Locate every Trypanosoma brucei.
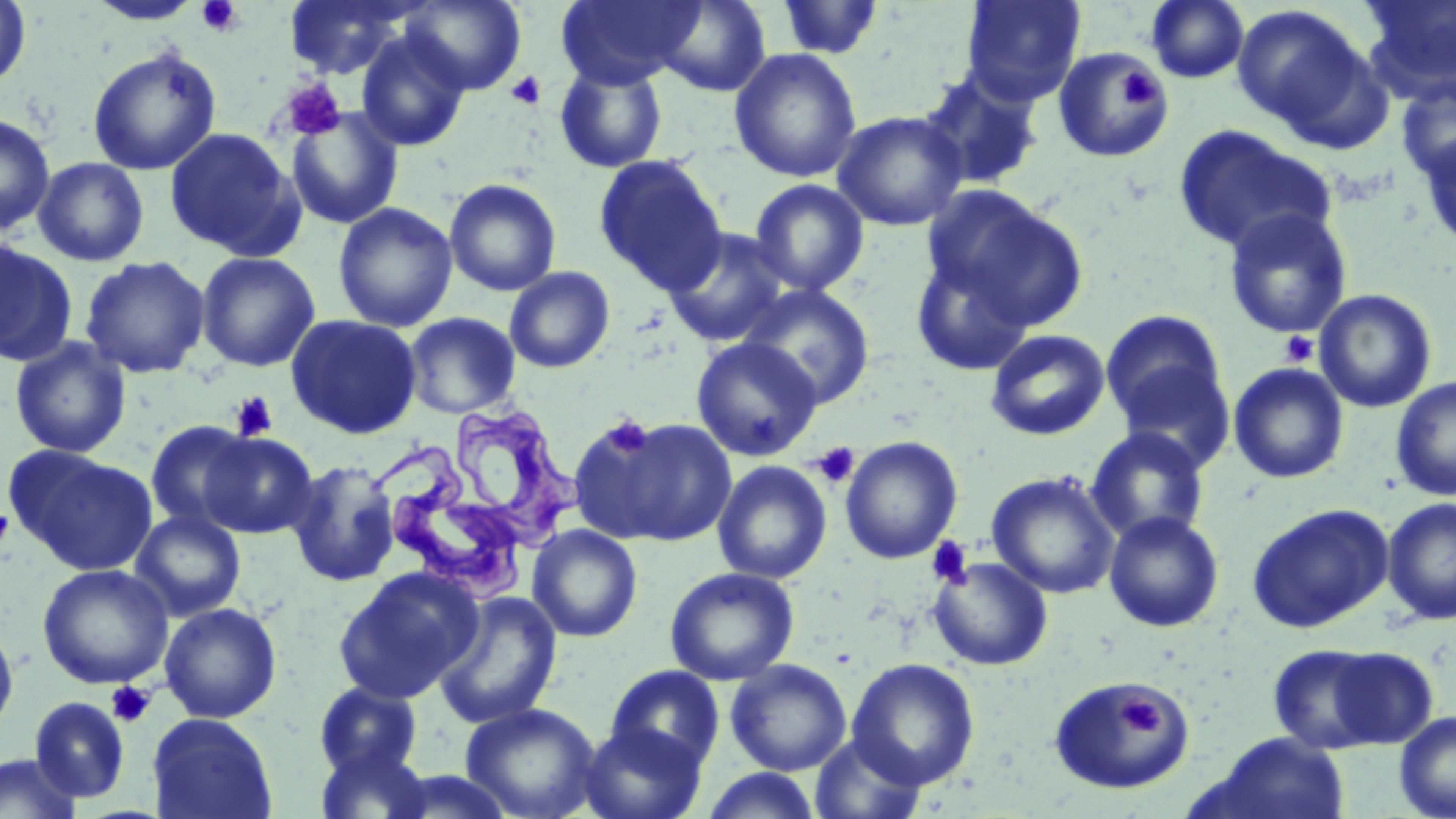
Approximate bounding boxes as (x1,y1)-(x2,y2) corner pairs in pixels.
Trypanosoma brucei: (440,410)-(585,556), (375,445)-(529,608).

slide-level diagnosis = Trypanosoma brucei
preparation = thin blood film
magnification = 1000x
platelet locations = approximate bounding boxes as (x1,y1)-(x2,y2) corner pairs in pixels: (196,0)-(243,37), (1116,67)-(1166,109), (505,70)-(547,110), (280,78)-(346,141), (1279,331)-(1319,367), (230,392)-(278,442), (601,416)-(653,459), (812,442)-(860,488), (0,506)-(15,551), (926,537)-(973,589), (107,682)-(155,728), (1120,696)-(1161,736)
modality = light microscopy
stain = May-Grünwald-Giemsa
field of view = one of a larger specimen
uninfected red blood cell locations = approximate bounding boxes as (x1,y1)-(x2,y2) corner pairs in pixels: (0,0)-(32,91), (86,0)-(205,25), (283,0)-(418,80), (400,0)-(527,95), (557,0)-(701,88), (653,0)-(771,97), (776,0)-(885,60), (960,0)-(1086,105), (1146,0)-(1249,84), (1359,0)-(1456,101), (1232,5)-(1377,140), (356,30)-(470,151), (87,46)-(221,176), (1052,47)-(1174,163), (729,48)-(862,183), (554,61)-(668,173), (916,69)-(1046,191), (1395,73)-(1456,186), (285,107)-(404,229), (832,110)-(968,232), (0,113)-(55,235), (1172,125)-(1334,256), (163,127)-(303,260), (1416,128)-(1456,254), (593,154)-(728,295), (33,157)-(150,267), (443,178)-(562,296), (750,179)-(869,297), (923,185)-(1088,331), (333,202)-(458,332), (1222,208)-(1353,340), (662,226)-(792,347), (0,240)-(77,366), (911,250)-(1035,377), (196,251)-(321,372), (80,256)-(210,379), (504,266)-(615,373), (738,283)-(874,409), (1314,289)-(1437,413), (1100,310)-(1228,430), (403,312)-(521,418), (285,314)-(422,439), (985,329)-(1110,441), (9,337)-(131,458), (690,337)-(822,461), (1112,360)-(1237,474), (1229,362)-(1348,483), (1390,376)-(1456,502), (574,415)-(735,546), (145,420)-(259,532), (1085,427)-(1210,545), (200,432)-(318,538), (840,435)-(963,564), (8,447)-(157,576), (287,459)-(402,587), (712,460)-(832,584), (986,471)-(1121,599), (1382,496)-(1456,626), (1246,503)-(1394,632), (130,509)-(246,621), (1103,510)-(1225,633), (527,524)-(643,642), (927,556)-(1053,671), (37,563)-(174,689), (332,565)-(484,704), (664,567)-(799,685), (433,591)-(563,729), (159,602)-(282,723), (0,621)-(18,736), (1266,643)-(1404,754), (846,658)-(980,789), (725,659)-(852,776), (605,665)-(725,771), (1049,677)-(1195,796), (314,681)-(423,779), (30,696)-(130,802), (460,702)-(602,819), (1394,710)-(1456,819), (147,713)-(277,819), (579,721)-(707,819), (808,732)-(928,818), (1204,732)-(1351,819), (315,741)-(433,819), (0,752)-(83,819), (700,767)-(824,818)
image size = 1456×819 pixels